Point out each leukocyte.
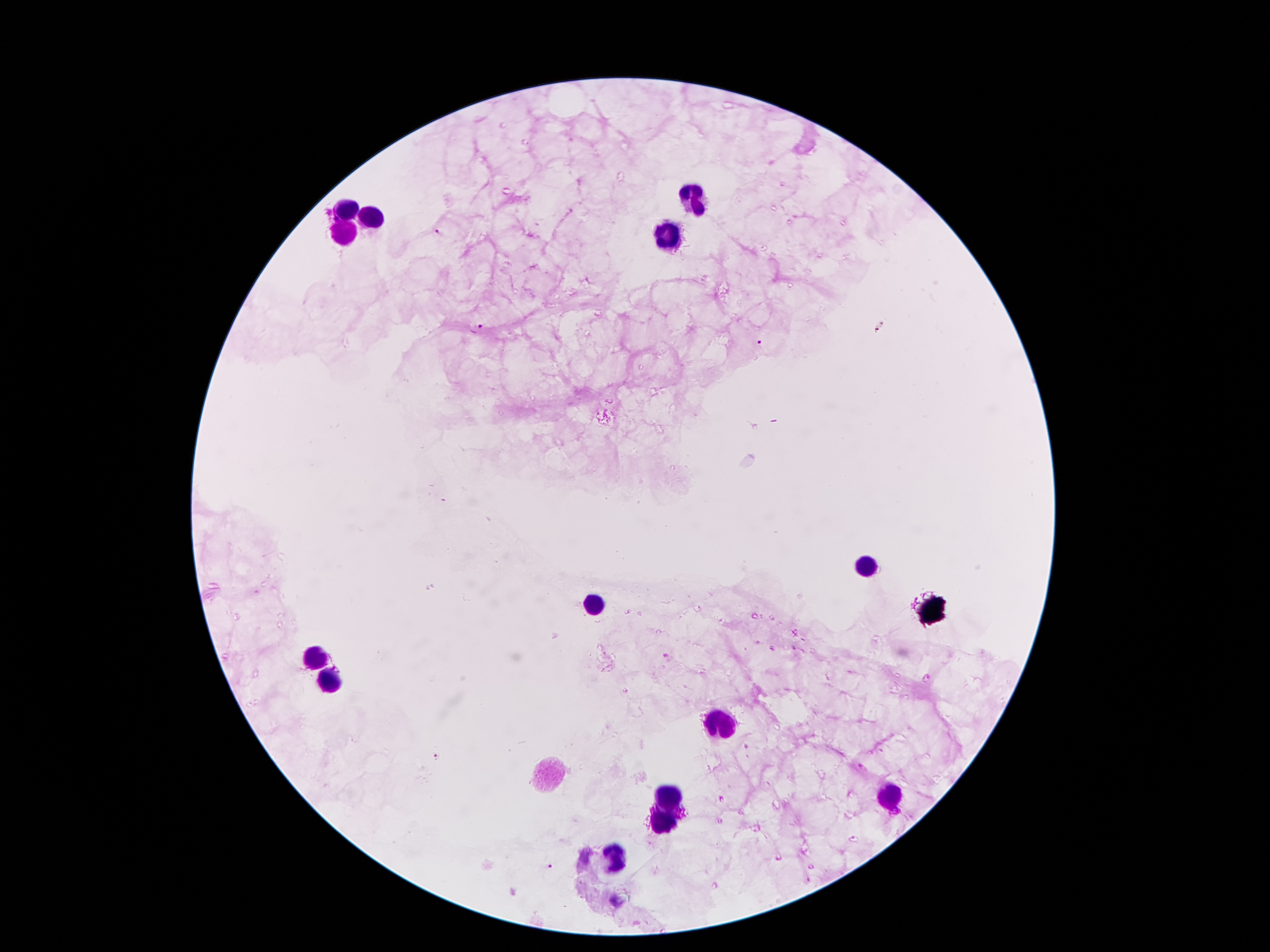

Approximate centers as (x, y) in pixels.
Leukocytes: (694, 198), (347, 211), (374, 217), (345, 232), (668, 240), (864, 567), (595, 603), (314, 658), (332, 685), (723, 723), (671, 796), (887, 796), (664, 819), (614, 861).

Plasmodium parasite locations: (438, 234), (478, 328), (757, 341), (438, 759), (548, 868). One field from this slide. Smartphone photograph taken through the microscope eyepiece. Thick blood smear. Image is 1270×952 pixels. 100x magnification. Giemsa stain. Patient malaria status: positive for Plasmodium falciparum.